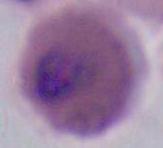
Summary:
  - Modality: photomicrograph
  - Identification: Plasmodium
  - Magnification: 400x or 1000x